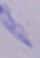

{
  "identification": "trypanosome",
  "magnification": "1000x",
  "modality": "photomicrograph"
}